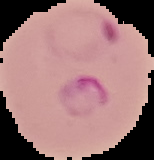
malaria_status: parasitized
image_size: 154×160 pixels
image_type: segmented cell region on a black background
preparation: thin blood smear